Identify the cell.
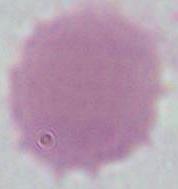

This is an erythrocyte.

Photomicrograph. Captured at 1000x magnification.